Outline each Plasmodium vivax-infected red blood cell.
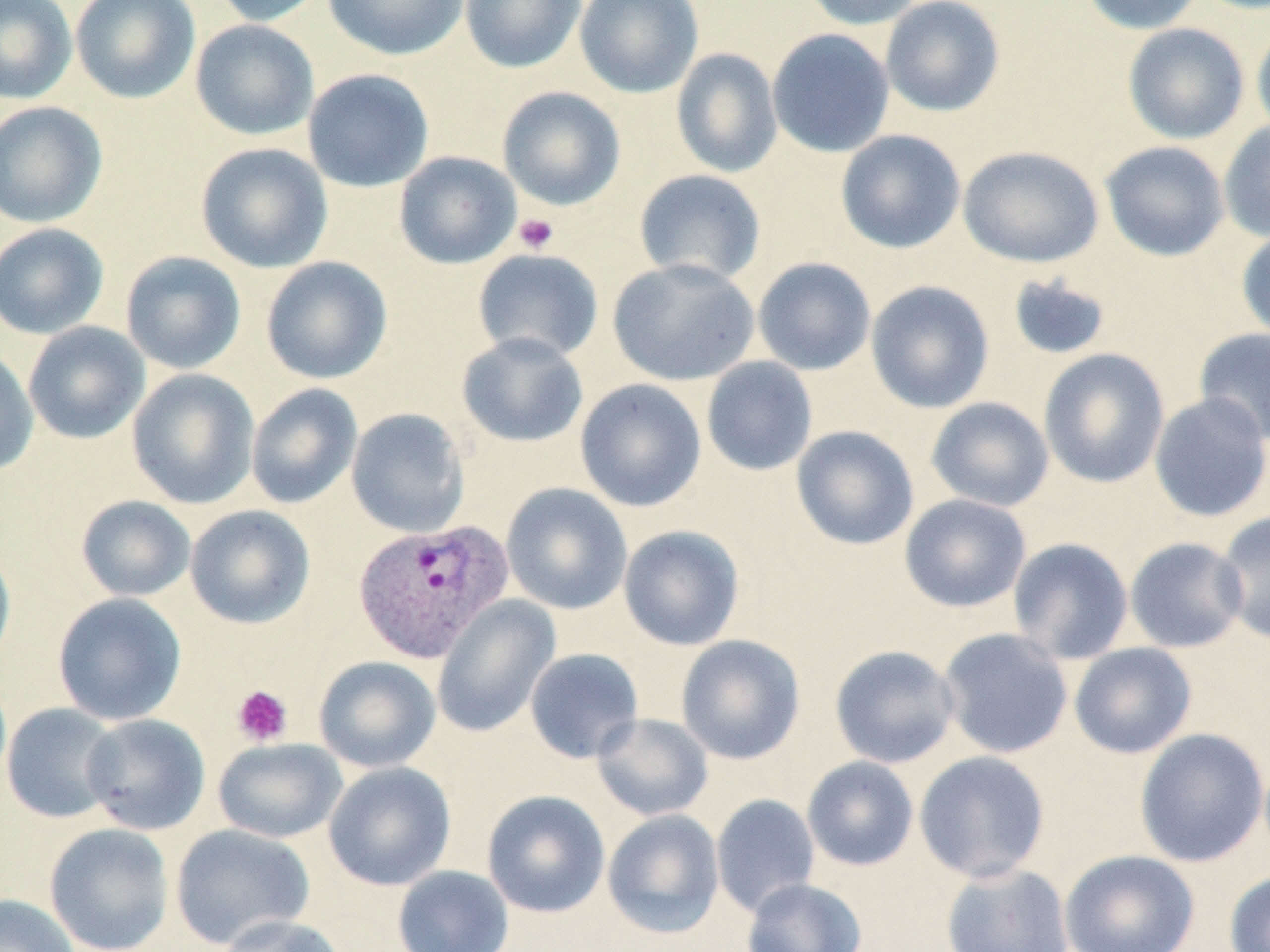
Approximate bounding boxes as [x1, y1, x2, y2] in pixels.
Plasmodium vivax-infected red blood cells: [356, 519, 519, 665].

slide-level diagnosis = Plasmodium vivax
modality = light microscopy
magnification = 1000x
platelet locations = approximate bounding boxes as [x1, y1, x2, y2] in pixels: [514, 213, 559, 254], [231, 684, 293, 746]
stain = May-Grünwald-Giemsa
uninfected red blood cell locations = approximate bounding boxes as [x1, y1, x2, y2] in pixels: [0, 0, 78, 104], [70, 0, 200, 104], [211, 0, 328, 27], [322, 0, 470, 60], [459, 0, 587, 73], [574, 0, 704, 98], [799, 0, 928, 30], [880, 0, 1005, 117], [1079, 0, 1205, 35], [190, 19, 319, 140], [1251, 20, 1270, 140], [1122, 23, 1249, 144], [767, 28, 895, 157], [671, 48, 783, 178], [302, 68, 434, 193], [496, 86, 626, 211], [0, 101, 108, 227], [1219, 119, 1270, 243], [835, 129, 966, 254], [1100, 141, 1230, 261], [195, 142, 333, 273], [958, 145, 1104, 268], [394, 150, 522, 269], [634, 169, 766, 285], [0, 223, 109, 339], [1236, 228, 1270, 343], [472, 248, 604, 363], [121, 251, 246, 374], [260, 256, 392, 384], [753, 257, 876, 376], [607, 258, 759, 386], [1006, 272, 1114, 361], [866, 280, 995, 413], [23, 321, 150, 444], [1194, 327, 1270, 446], [457, 332, 589, 448], [0, 347, 39, 477], [1038, 348, 1170, 488], [701, 356, 817, 476], [127, 369, 260, 509], [575, 378, 706, 512], [246, 383, 363, 509], [1149, 392, 1270, 523], [926, 397, 1054, 511], [346, 408, 470, 537], [790, 425, 919, 551], [500, 483, 632, 615], [899, 494, 1031, 612], [75, 495, 196, 602], [185, 504, 315, 629], [1215, 511, 1270, 644], [618, 525, 745, 650], [1007, 537, 1133, 665], [1125, 537, 1248, 653], [0, 541, 16, 672], [52, 593, 187, 726], [431, 596, 561, 737], [937, 627, 1073, 759], [676, 634, 805, 764], [1069, 642, 1197, 759], [829, 644, 960, 768], [525, 648, 644, 763], [313, 656, 441, 773], [1, 703, 121, 823], [80, 713, 211, 835], [592, 713, 714, 821], [1134, 728, 1268, 867], [212, 737, 347, 843], [914, 750, 1050, 882], [802, 756, 919, 871], [323, 761, 456, 891], [481, 790, 610, 918], [711, 793, 820, 917], [602, 809, 725, 939], [43, 822, 174, 952], [170, 823, 315, 949], [1059, 849, 1200, 952], [940, 862, 1075, 952], [393, 864, 514, 952], [1224, 870, 1270, 952], [741, 878, 868, 952], [0, 893, 81, 952], [216, 914, 348, 952]
preparation = thin blood smear
image size = 1270×952 pixels
field of view = one of a larger specimen